Outline each blood parasite and name the species.
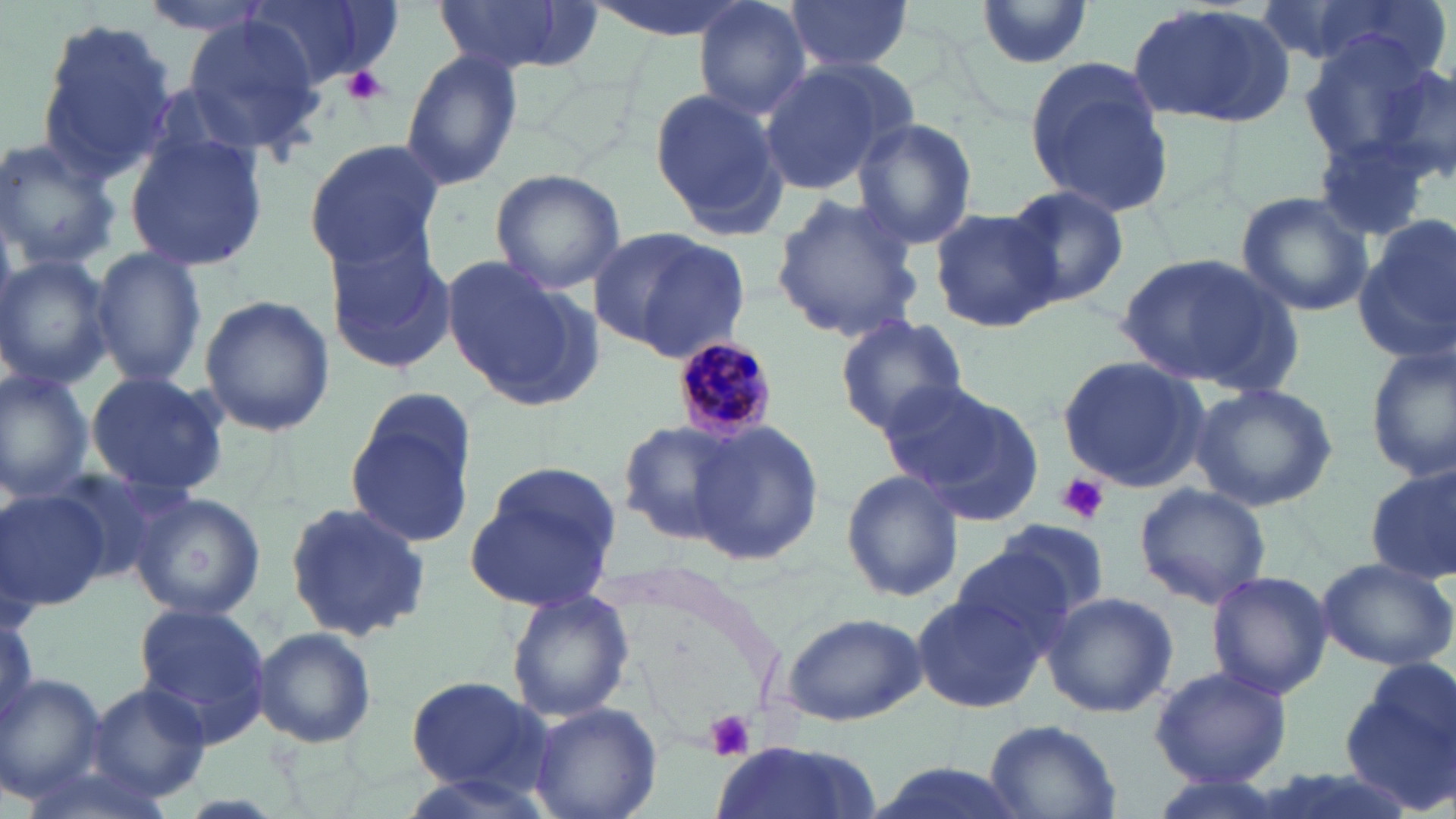

Approximate bounding boxes as (x1,y1)-(x2,y2) corner pairs in pixels.
Plasmodium malariae-infected red blood cells: (670,336)-(779,443).
No Plasmodium falciparum, Plasmodium ovale, Plasmodium vivax, Babesia divergens, or Trypanosoma brucei observed.

Uninfected red blood cell locations: (139,0)-(279,37), (242,0)-(389,90), (432,0)-(588,75), (784,0)-(915,74), (976,0)-(1091,67), (1278,0)-(1454,83), (693,1)-(811,121), (1125,4)-(1295,128), (34,19)-(176,179), (182,19)-(326,155), (1297,27)-(1444,172), (400,47)-(523,192), (1371,58)-(1456,188), (756,59)-(909,198), (1022,60)-(1172,215), (649,85)-(790,233), (851,118)-(979,249), (125,133)-(267,274), (0,137)-(120,276), (1315,138)-(1436,243), (301,139)-(444,273), (488,168)-(627,293), (1003,185)-(1130,309), (1235,190)-(1374,317), (768,192)-(922,341), (930,208)-(1061,331), (1355,218)-(1455,361), (590,226)-(749,357), (324,233)-(457,378), (90,245)-(209,387), (1115,252)-(1302,397), (442,255)-(599,409), (0,256)-(115,390), (196,295)-(336,437), (835,314)-(969,437), (1366,343)-(1455,487), (1057,355)-(1209,492), (0,366)-(97,502), (84,371)-(230,496), (883,380)-(1047,523), (1187,381)-(1338,511), (343,390)-(479,551), (617,420)-(742,544), (689,420)-(824,568), (464,460)-(627,611), (841,466)-(962,603), (1365,467)-(1455,587), (53,468)-(188,582), (1134,485)-(1271,609), (0,486)-(111,611), (130,491)-(265,621), (282,499)-(434,642), (992,517)-(1114,620), (950,548)-(1076,658), (1315,556)-(1455,673), (1204,570)-(1333,699), (508,590)-(634,721), (910,590)-(1049,715), (1040,592)-(1178,719), (133,603)-(273,744), (0,605)-(36,731), (781,610)-(926,726), (253,627)-(378,749), (1340,658)-(1456,809), (1149,665)-(1293,788), (0,674)-(107,803), (404,675)-(550,793), (85,681)-(215,807), (525,701)-(662,819), (982,719)-(1121,818), (708,741)-(881,819), (863,759)-(1034,819). Platelet locations: (342,67)-(388,106), (1054,473)-(1111,525), (705,708)-(757,761). Slide-level diagnosis: Plasmodium malariae. Single field of view. Captured at 1000x magnification. Thin blood film. May-Grünwald-Giemsa stain. Optical microscopy. Image is 1456×819 pixels.